Classify this cell by malaria status.
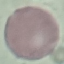
Uninfected.

Summary:
  - Stain: Giemsa
  - Capture: smartphone through the microscope eyepiece
  - Preparation: thin smear
  - Image type: automatically extracted cell patch, resized to 64 × 64 pixels